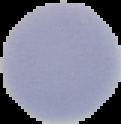

Summary:
  - Image type: segmented cell region with the area outside set to black
  - Preparation: thin blood film
  - Image size: 121×124 pixels
  - Malaria status: uninfected